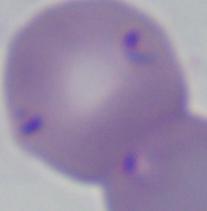 A Babesia parasite is seen. Captured at 1000x magnification. Photomicrograph.